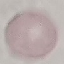
Malaria status: uninfected. Cell patch, automatically extracted from a larger field of view and resized to 64 × 64 pixels. Giemsa stain. Thin smear of blood. Acquired by smartphone through the microscope eyepiece.